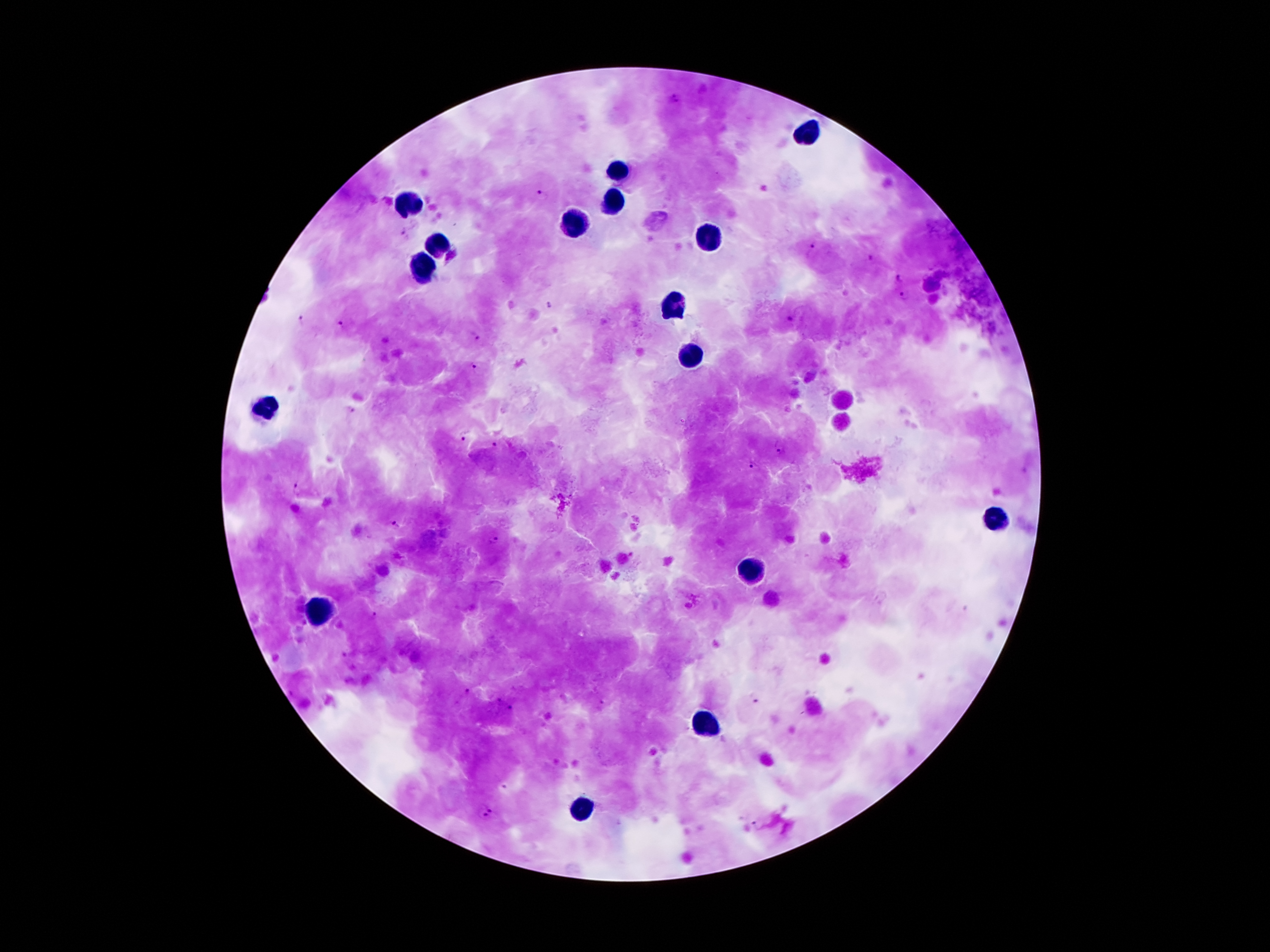 Approximate centers as {x, y} in pixels. Leukocyte locations: {805, 133}, {619, 173}, {615, 199}, {409, 204}, {577, 223}, {713, 237}, {440, 243}, {423, 267}, {673, 306}, {691, 355}, {267, 403}, {996, 516}, {748, 569}, {316, 613}, {703, 723}, {582, 804}. Malaria parasite locations: {673, 97}, {542, 194}, {405, 232}, {813, 249}, {869, 256}, {897, 278}, {903, 296}, {549, 304}, {299, 317}, {792, 317}, {341, 325}, {474, 335}, {475, 366}, {352, 409}, {463, 435}, {496, 444}, {779, 447}, {752, 467}, {295, 486}, {395, 523}, {494, 541}, {374, 616}, {467, 692}, {754, 698}, {498, 700}, {602, 704}, {509, 708}, {488, 811}, {757, 824}. Smartphone photograph taken through the microscope eyepiece. Image is 1270×952 pixels. Thick peripheral-blood smear. 100x magnification. Patient malaria status: positive for Plasmodium falciparum. Single field of view. Giemsa-stained preparation.